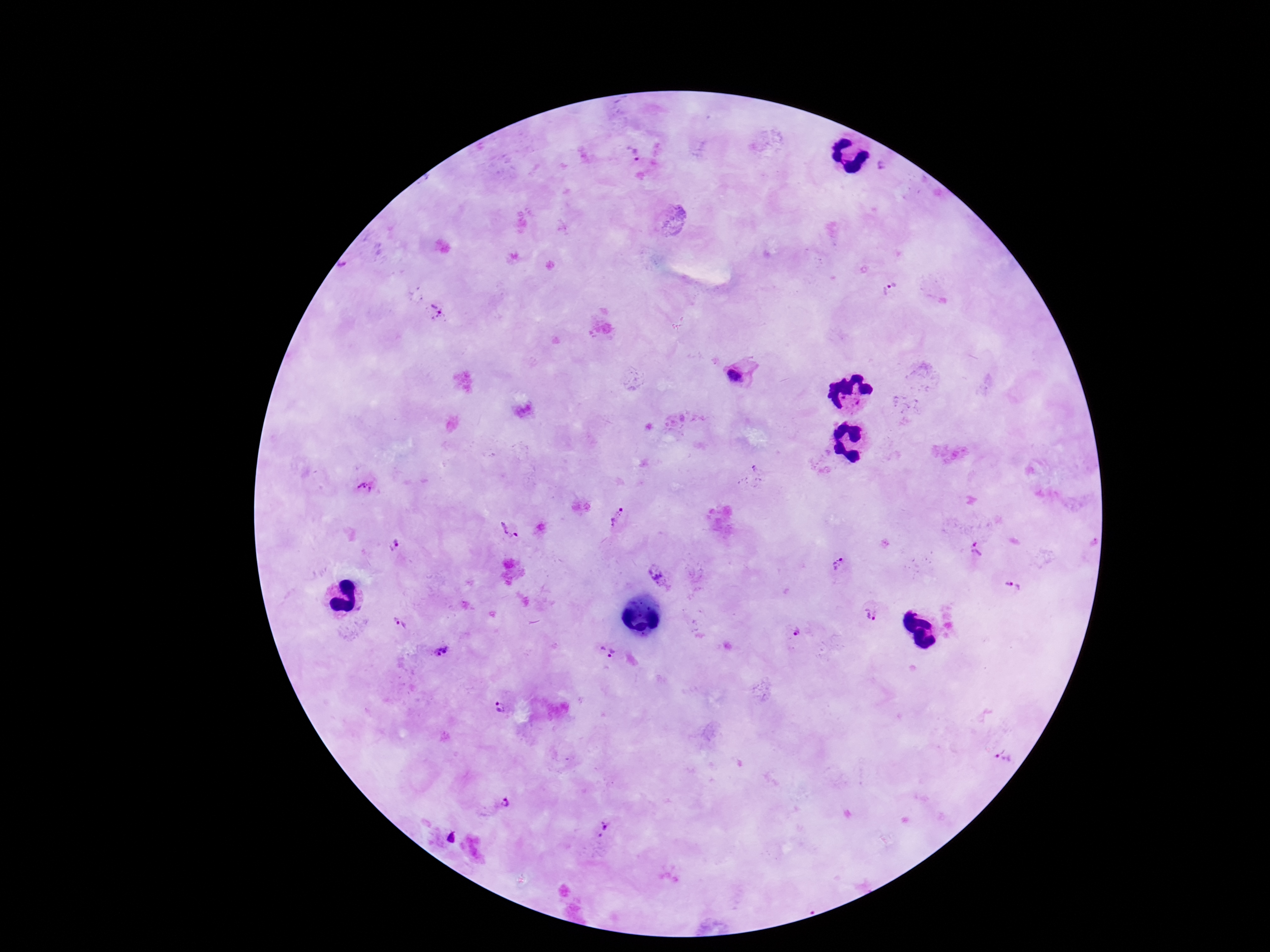

Approximate centers as (x, y) in pixels. Plasmodium parasite locations: (631, 154), (881, 166), (350, 269), (891, 288), (435, 313), (740, 372), (364, 489), (617, 518), (507, 529), (393, 546), (975, 548), (839, 564), (657, 574), (1013, 586), (872, 609), (398, 625), (794, 632), (607, 652), (442, 653), (498, 708), (1007, 756), (505, 803), (605, 828). Single field of view. Image is 1270×952 pixels. 100x magnification. Smartphone photograph taken through the microscope eyepiece. Giemsa stain. Patient malaria status: positive. Thick blood smear.